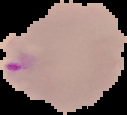

image_type: segmented cell region with the area outside set to black
malaria_status: parasitized
preparation: thin blood film
image_size: 127×115 pixels